Locate every leukocyte (white blood cell).
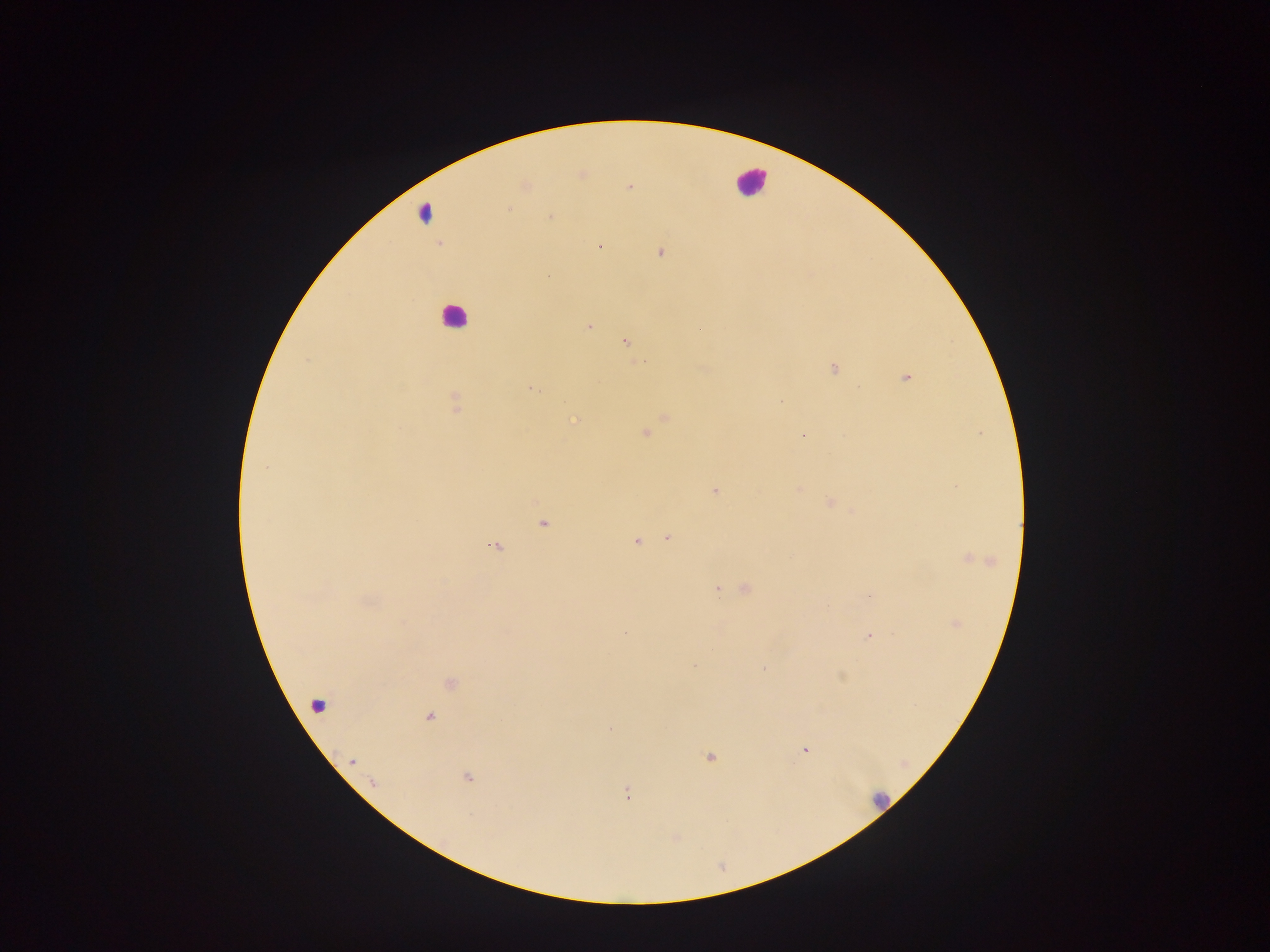
Approximate centers as (x, y) in pixels.
Leukocytes: (748, 184), (450, 316).

Plasmodium parasite locations: (509, 209), (551, 216), (598, 247), (660, 251), (549, 275), (590, 326), (626, 341), (833, 369), (907, 377), (530, 388), (455, 402), (574, 419), (645, 432), (803, 434), (264, 464), (799, 488), (717, 490), (829, 502), (543, 524), (669, 536), (637, 542), (494, 546), (965, 557), (746, 589), (717, 590), (867, 596), (625, 633), (867, 636), (764, 668), (840, 676), (449, 681), (429, 718), (804, 749), (708, 757), (470, 777), (629, 791). Single field of view. Mobile-phone photograph taken through the microscope. Collected in Ghana. Thick blood smear. Image is 1270×952 pixels.